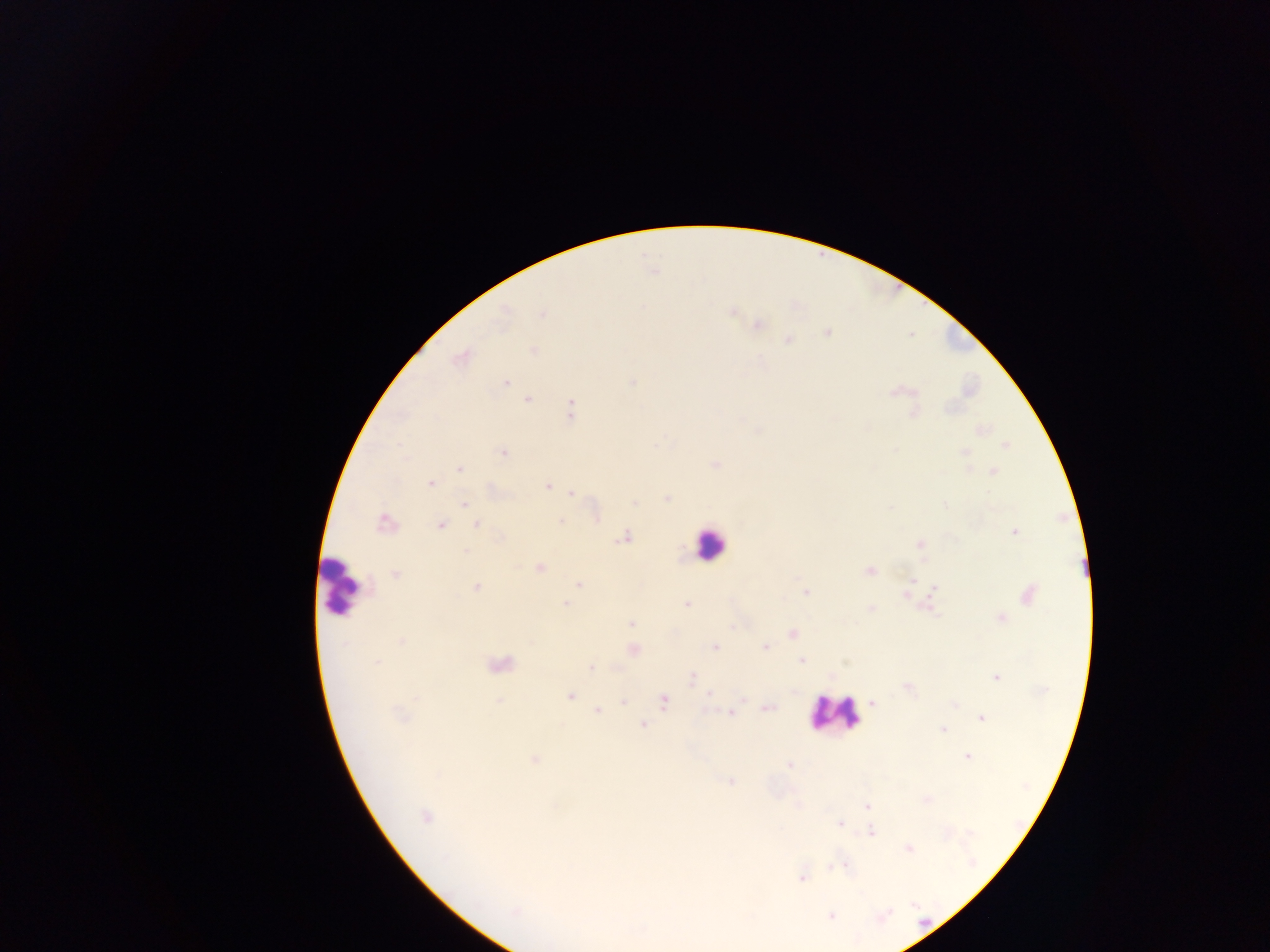
malaria parasite locations = approximate centers as [x, y] in pixels: [506, 384], [527, 399], [571, 405], [570, 414], [501, 452], [458, 469], [433, 483], [548, 486], [566, 491], [572, 494], [635, 502], [465, 504], [596, 517], [560, 520], [440, 526], [476, 526], [1014, 533], [626, 536], [465, 551], [539, 566], [578, 583], [911, 583], [476, 588], [933, 589], [804, 592], [686, 604], [565, 605], [934, 610], [631, 624], [792, 634], [716, 646], [766, 647], [801, 661], [377, 662], [591, 668], [995, 676], [692, 679], [569, 695], [709, 695], [873, 700], [623, 702], [664, 702], [767, 708], [596, 710], [732, 713], [980, 718], [642, 725], [942, 729], [967, 756], [789, 765], [731, 782], [866, 806], [425, 816], [838, 823], [871, 831], [908, 850], [844, 866], [832, 868], [802, 878], [514, 911], [831, 916]
leukocyte locations = approximate centers as [x, y] in pixels: [705, 545], [345, 585], [828, 709]
image size = 1270×952 pixels
capture = mobile-phone photograph through a microscope
field of view = single
country = Ghana
preparation = thick blood film